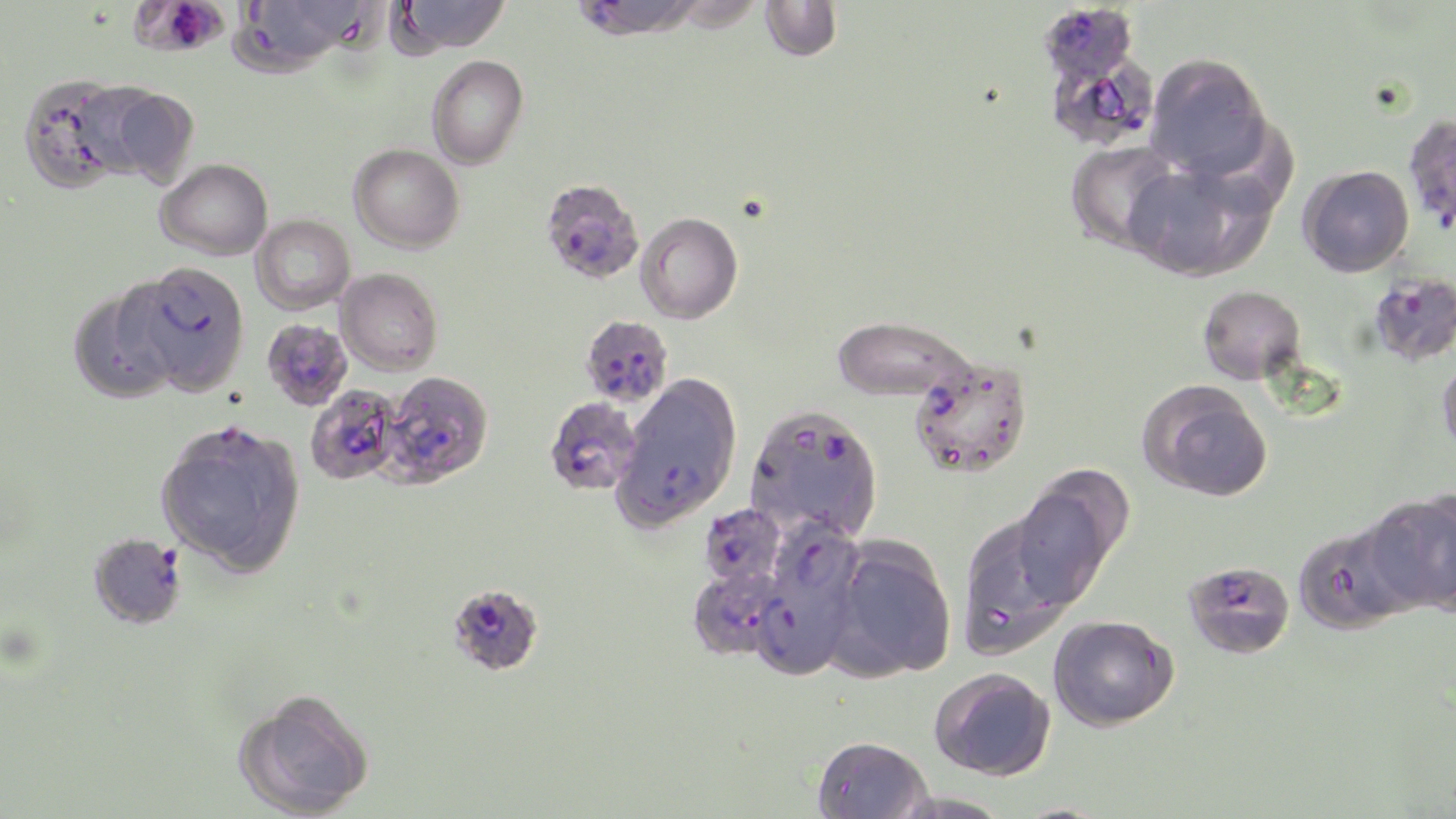

Summary:
  - Coordinate format: approximate bounding boxes as (x1,y1)-(x2,y2) corner pairs in pixels
  - Platelet locations: (159,1)-(222,54)
  - Plasmodium falciparum-infected red blood cell locations: (569,0)-(702,42), (1036,2)-(1140,86), (1049,52)-(1156,145), (540,177)-(645,285), (126,260)-(251,397), (1368,270)-(1456,367), (579,315)-(673,408), (260,318)-(352,411), (908,355)-(1033,479), (378,370)-(494,489), (618,376)-(742,524), (305,385)-(404,486), (544,396)-(643,496), (745,402)-(884,542), (699,503)-(787,589), (768,515)-(864,622), (88,532)-(187,630), (1182,559)-(1295,659), (688,566)-(787,661), (451,583)-(550,676), (751,592)-(850,682)
  - Uninfected red blood cell locations: (254,0)-(361,65), (305,0)-(397,56), (392,0)-(512,54), (759,1)-(842,62), (1145,52)-(1271,178), (426,54)-(528,169), (18,74)-(135,193), (96,84)-(199,186), (1403,113)-(1456,233), (1065,140)-(1181,253), (349,143)-(464,254), (155,158)-(273,260), (1126,159)-(1275,281), (1298,165)-(1414,277), (636,212)-(743,324), (251,215)-(355,315), (336,268)-(443,375), (67,285)-(179,405), (1198,285)-(1306,384), (831,315)-(978,405), (1437,357)-(1456,460), (1137,380)-(1273,502), (155,419)-(307,577), (1010,475)-(1127,608), (1363,491)-(1456,616), (954,509)-(1082,658), (1292,521)-(1417,635), (827,537)-(957,681), (1048,614)-(1179,732), (929,667)-(1057,780), (234,687)-(376,818), (812,735)-(932,819)
  - Slide-level diagnosis: Plasmodium falciparum
  - Magnification: 1000x
  - Modality: light microscopy
  - Preparation: thin blood smear
  - Field of view: one of a larger specimen
  - Stain: May-Grünwald-Giemsa
  - Image size: 1456×819 pixels